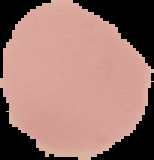

Summary:
  - Image type: segmented cell region with the area outside set to black
  - Preparation: thin blood film
  - Malaria status: uninfected
  - Image size: 154×160 pixels